Describe the morphology of the erythrocytes.
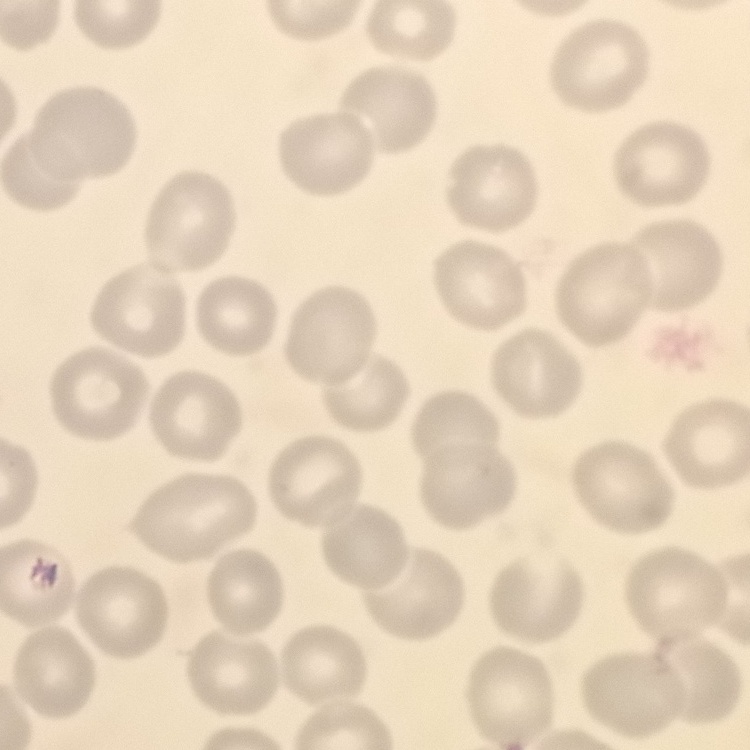

No rouleaux formation.

Summary:
  - Image type: one tile cut from a larger photomicrograph
  - Preparation: thin blood film
  - Stain: Field's or Giemsa